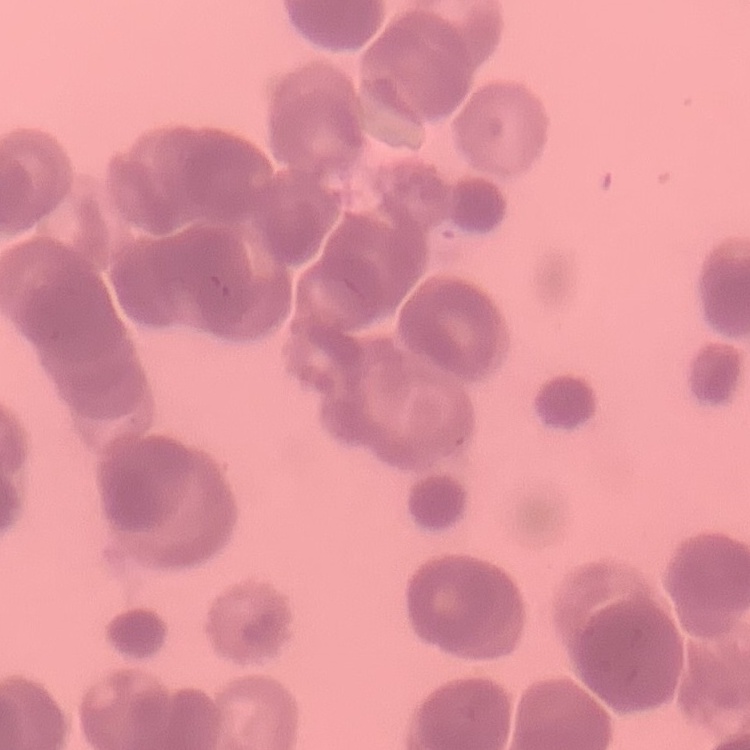
The red blood cells exhibit rouleaux formation. Field's or Giemsa stain. Thin blood smear. Square crop of a larger photomicrograph.